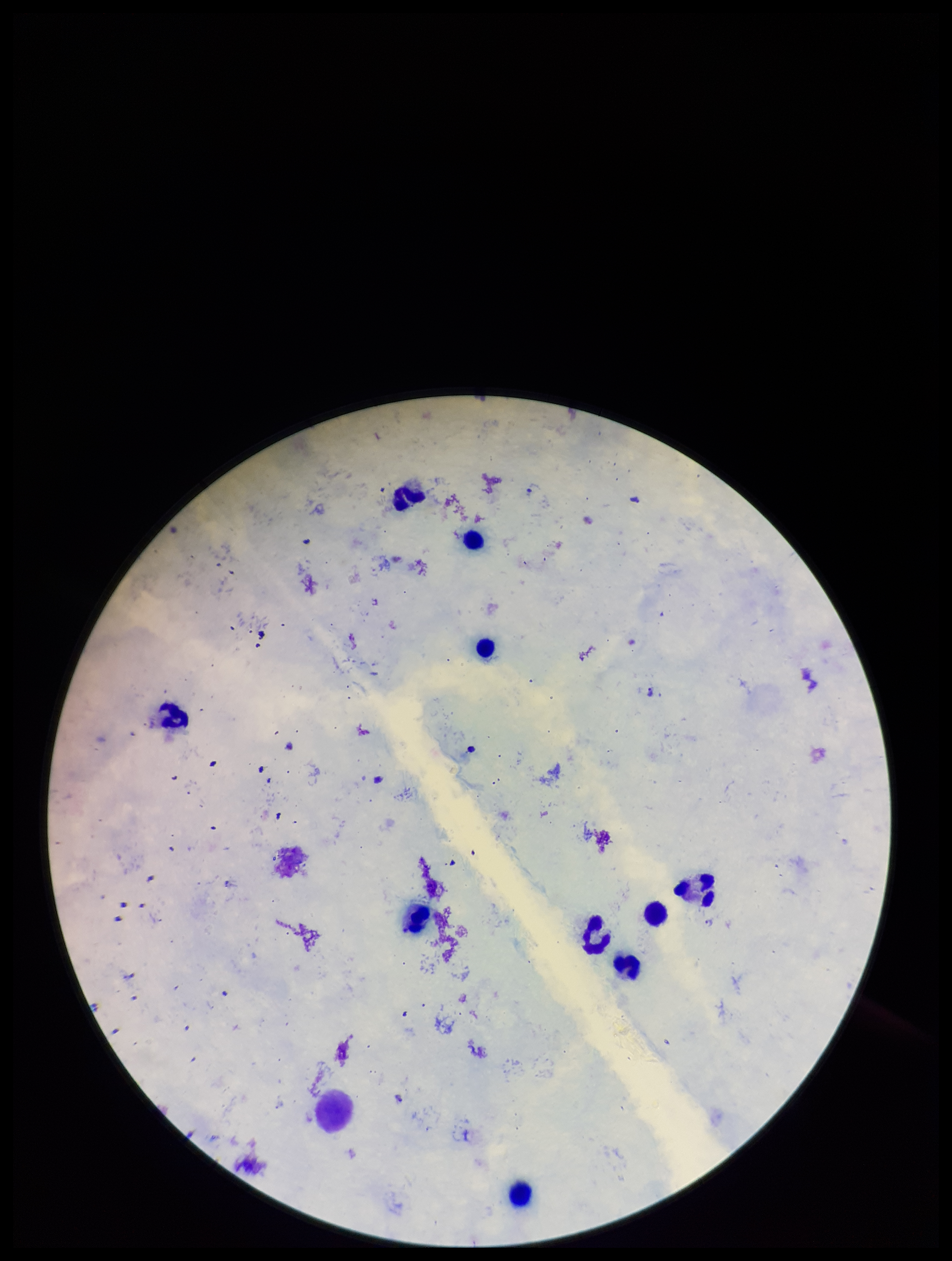

Summary:
  - Leukocyte count: 10
  - Parasite count: 3
  - Image size: 952×1261 pixels
  - Capture: smartphone photograph through the microscope eyepiece
  - Species reported for this patient: Plasmodium falciparum
  - Patient malaria status: infected
  - Field of view: single
  - Preparation: thick blood smear
  - Stain: Giemsa
  - Plasmodium parasites: seen